Assess this cell for malaria.
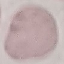

It is uninfected.

Giemsa stain. Acquired by smartphone through the microscope eyepiece. Thin blood smear. Cell patch, automatically extracted from a larger field of view and resized to 64 × 64 pixels.